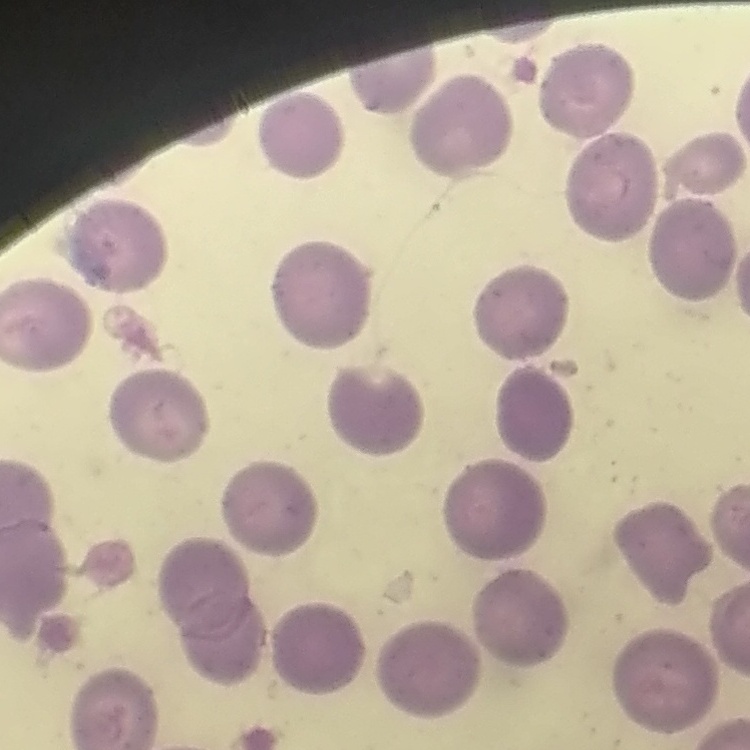
{
  "red_blood_cell_morphology": "no rouleaux formation",
  "stain": "Field's or Giemsa",
  "preparation": "thin blood film",
  "image_type": "one tile cut from a larger photomicrograph"
}